Evaluate for malaria.
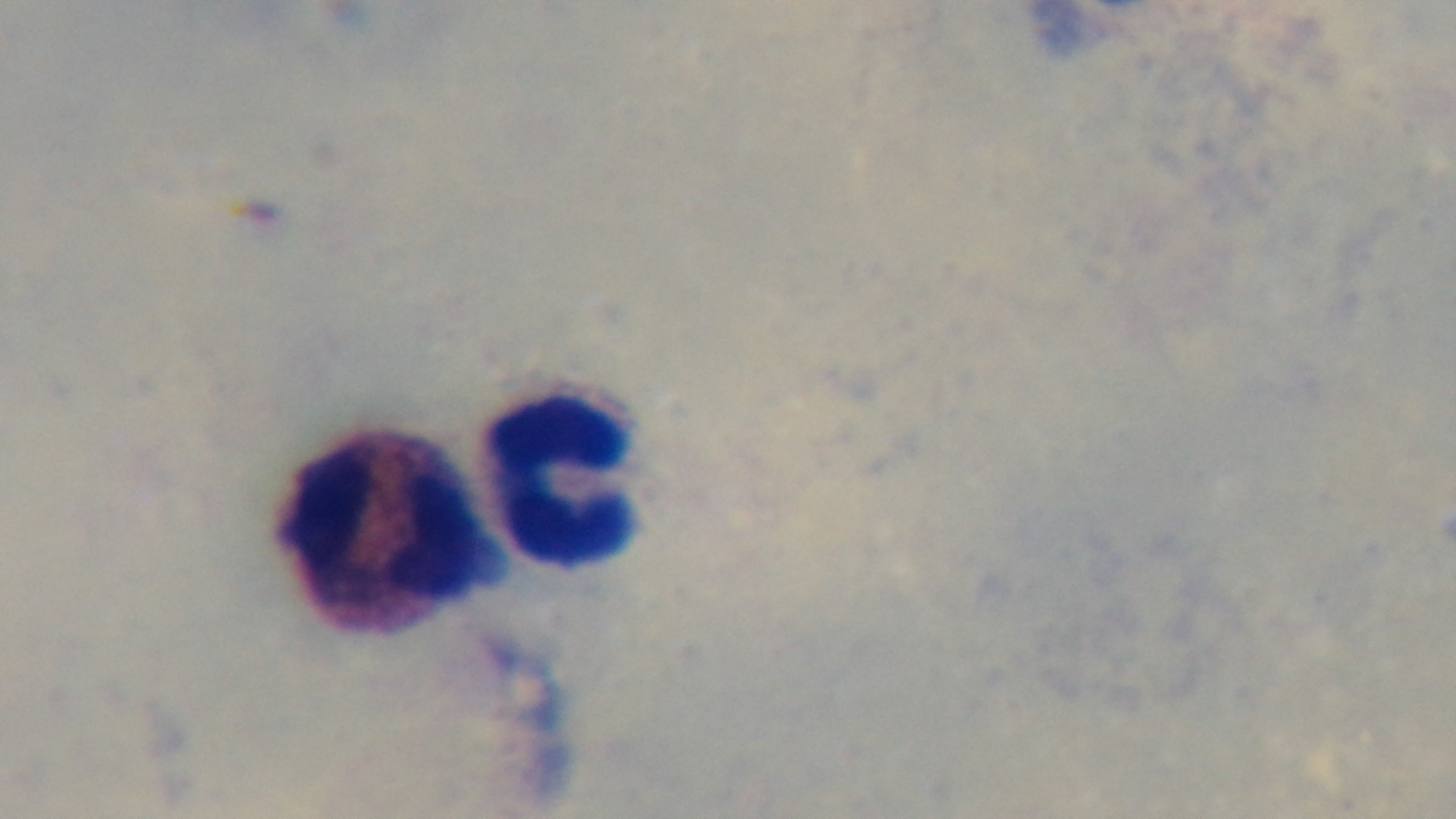
Negative.

Preparation: thick smear. Photomicrograph. 100x oil-immersion objective. Giemsa stain. One field from the slide. Mounted 4K digital camera.